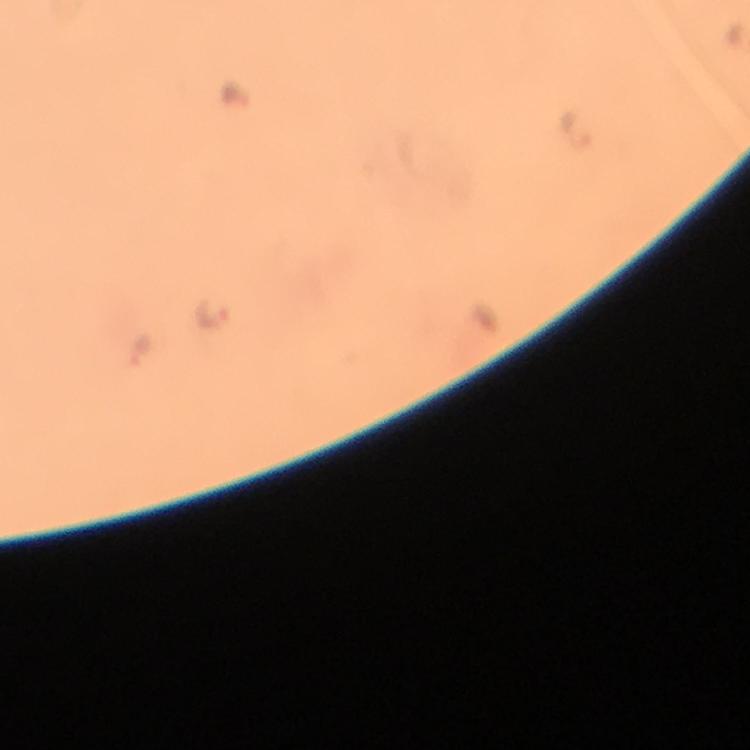

capture = smartphone camera through the microscope
preparation = thick blood smear
stain = Giemsa
immersion oil = used
context = from a diagnostic examination for malaria
image size = 750×750 pixels
cropped from = one field of view
magnification = 100x
Plasmodium parasite locations = approximate centers as {x, y} in pixels: {576, 132}, {211, 314}, {140, 354}